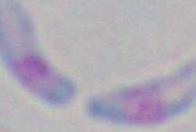 Toxoplasma gondii is seen. Photomicrograph. 1000x magnification.